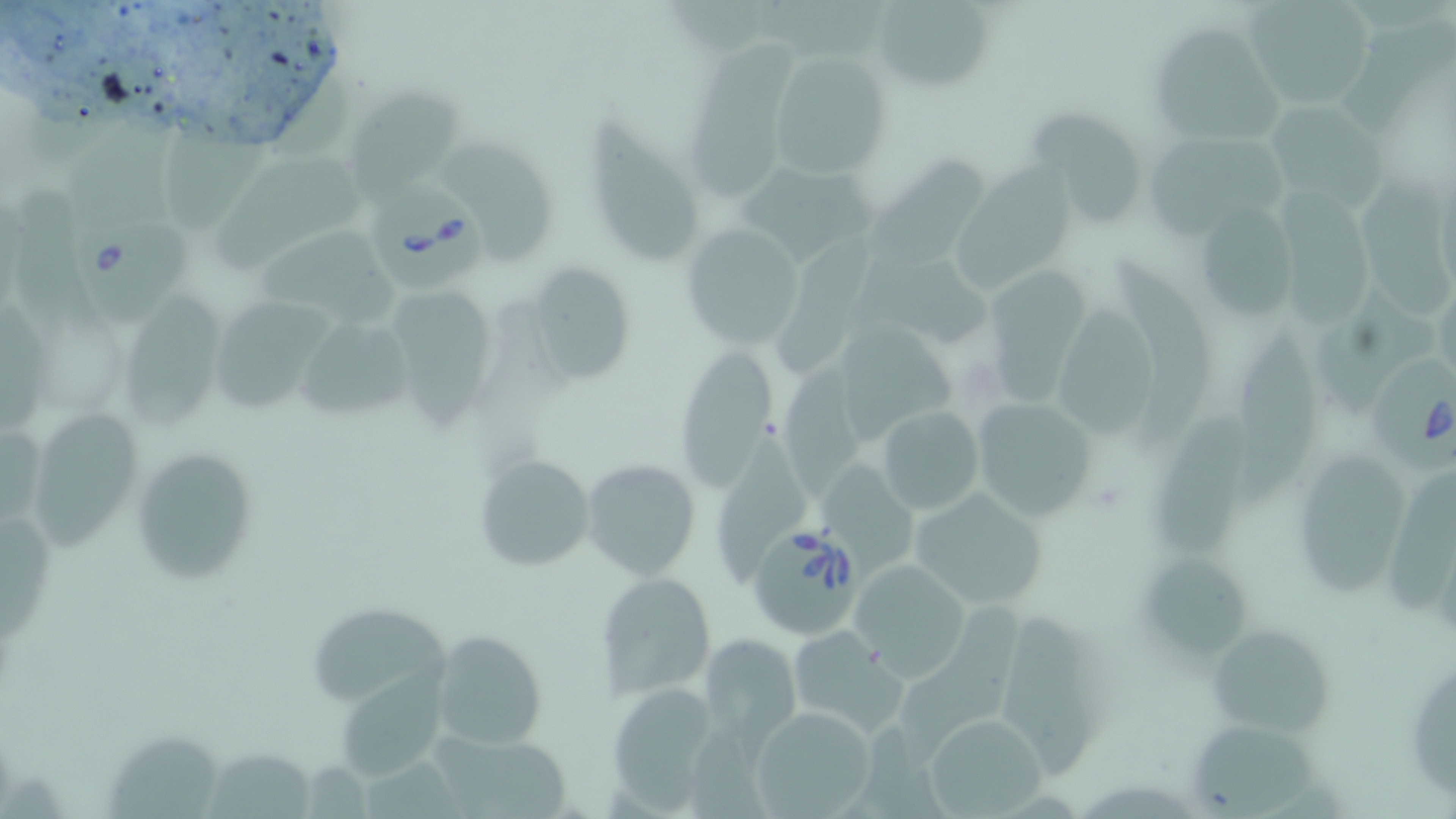
slide-level diagnosis = Babesia divergens
modality = optical microscopy
uninfected red blood cell locations = approximate bounding boxes as [x1, y1, x2, y2] in pixels: [748, 0, 881, 55], [1241, 0, 1375, 109], [872, 1, 997, 93], [1338, 17, 1456, 139], [1149, 23, 1284, 153], [691, 34, 793, 197], [768, 51, 892, 181], [350, 82, 461, 199], [1262, 100, 1388, 210], [1031, 108, 1151, 228], [593, 111, 703, 263], [68, 116, 182, 234], [164, 126, 266, 238], [1142, 128, 1291, 239], [444, 141, 556, 264], [859, 148, 983, 263], [215, 154, 370, 265], [953, 157, 1081, 291], [742, 158, 876, 261], [1359, 167, 1450, 321], [1270, 176, 1372, 334], [13, 189, 103, 341], [1194, 202, 1299, 323], [260, 223, 406, 328], [678, 224, 806, 348], [772, 226, 873, 365], [852, 254, 996, 344], [1117, 257, 1220, 455], [523, 263, 636, 386], [983, 264, 1086, 407], [397, 286, 498, 425], [1320, 287, 1436, 411], [126, 289, 222, 432], [223, 297, 333, 412], [1, 298, 52, 435], [1060, 303, 1162, 443], [294, 316, 415, 421], [1235, 318, 1322, 508], [836, 319, 957, 434], [677, 348, 775, 487], [781, 355, 872, 496], [967, 393, 1102, 525], [873, 402, 987, 519], [31, 403, 142, 551], [1162, 409, 1250, 558], [711, 435, 810, 576], [1297, 441, 1404, 598], [130, 447, 258, 586], [474, 452, 597, 574], [580, 457, 701, 581], [819, 464, 923, 573], [1390, 474, 1452, 617], [907, 487, 1049, 610], [0, 516, 54, 642], [1145, 549, 1258, 659], [850, 561, 971, 675], [598, 572, 714, 699], [898, 598, 1026, 764], [310, 600, 455, 701], [1009, 610, 1105, 778], [1204, 621, 1333, 738], [789, 625, 905, 737], [429, 630, 548, 750], [701, 633, 800, 741], [1406, 647, 1455, 805], [339, 653, 453, 778], [605, 684, 721, 809], [750, 704, 877, 817], [925, 713, 1047, 819], [841, 719, 953, 819], [1189, 723, 1329, 819], [102, 725, 221, 819], [431, 728, 575, 819], [688, 733, 779, 819], [209, 748, 316, 817], [365, 759, 473, 819]
Babesia divergens-infected red blood cell locations = approximate bounding boxes as [x1, y1, x2, y2] in pixels: [370, 182, 492, 296], [72, 216, 189, 322], [1367, 349, 1452, 475], [751, 523, 863, 635]
field of view = single
preparation = thin blood film
image size = 1456×819 pixels
magnification = 1000x
stain = May-Grünwald-Giemsa